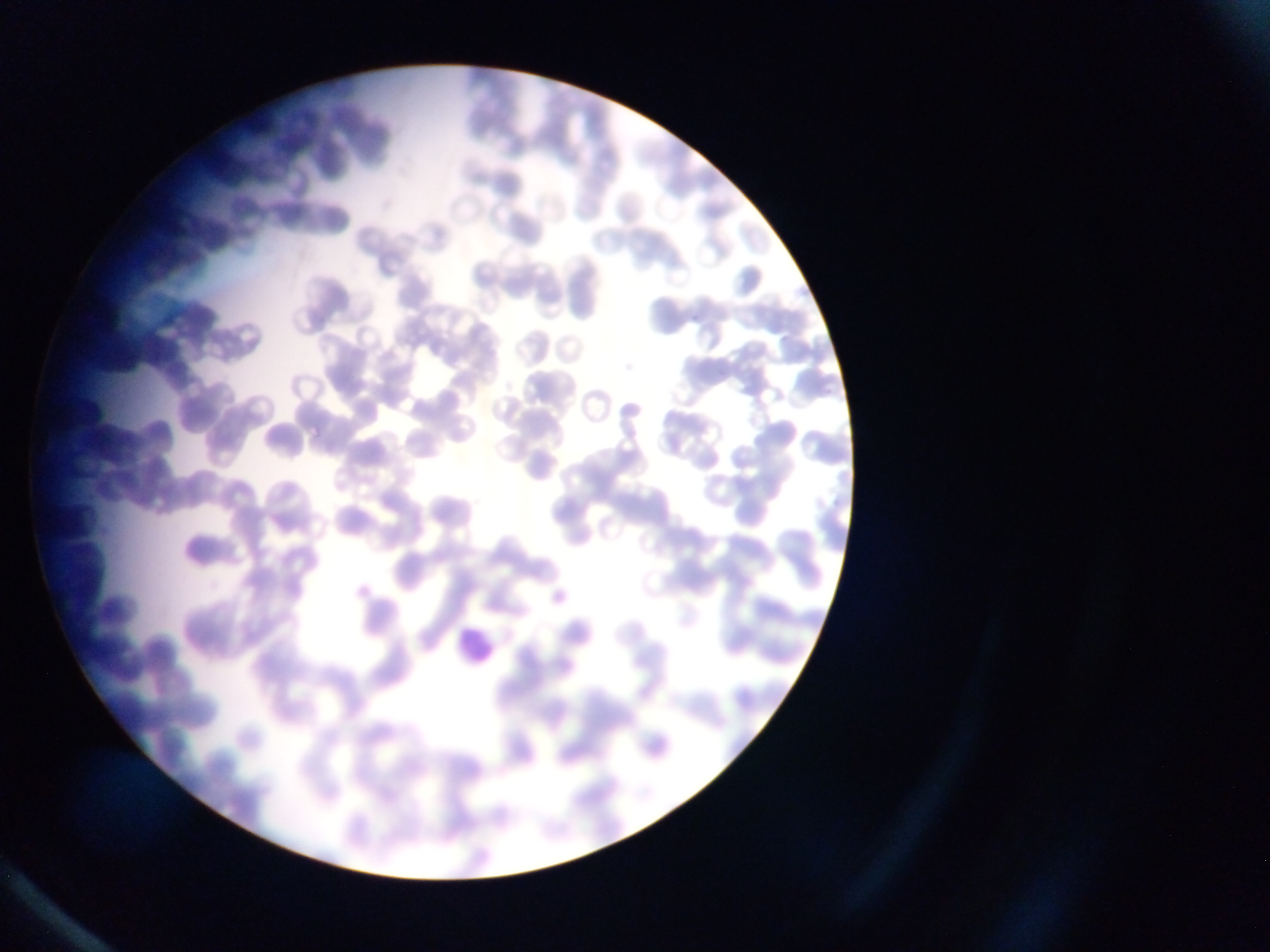
Approximate bounding boxes as left top right bottom in pixels. Leukocyte locations: 450 621 498 671. One field of view. Image is 1270×952 pixels. Thin blood smear. Sample from Ghana. Mobile-phone photograph taken through the microscope.